Comment on the morphology of the erythrocytes.
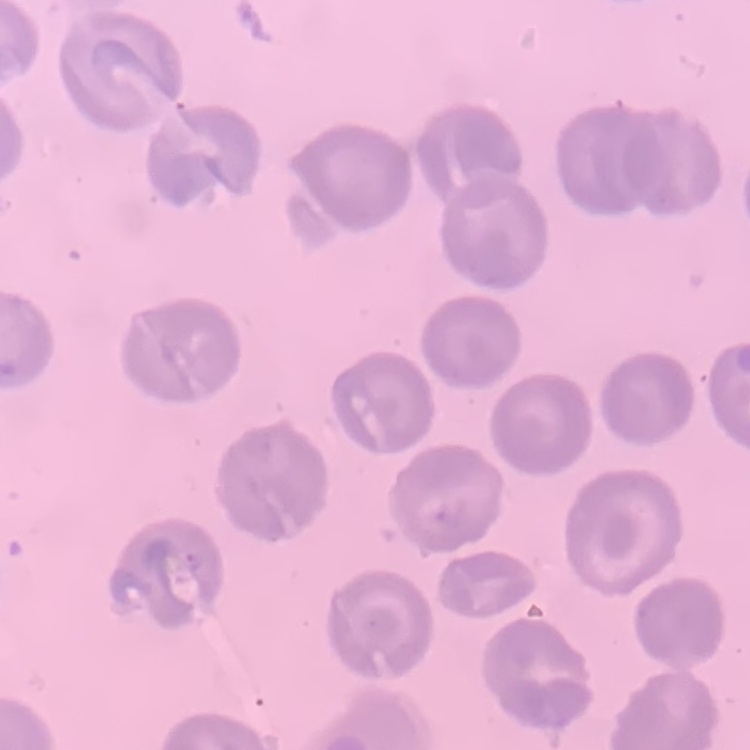
They show no rouleaux formation.

image_type: one tile cut from a larger photomicrograph
preparation: thin peripheral smear
stain: Field's or Giemsa